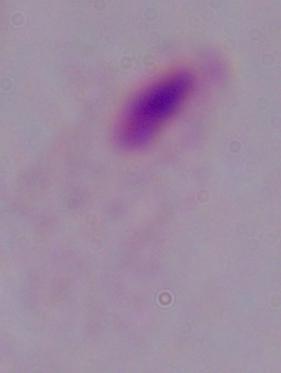

Summary:
  - Modality: micrograph
  - Magnification: 1000x
  - Identification: trichomonad